Identify the preparation type.
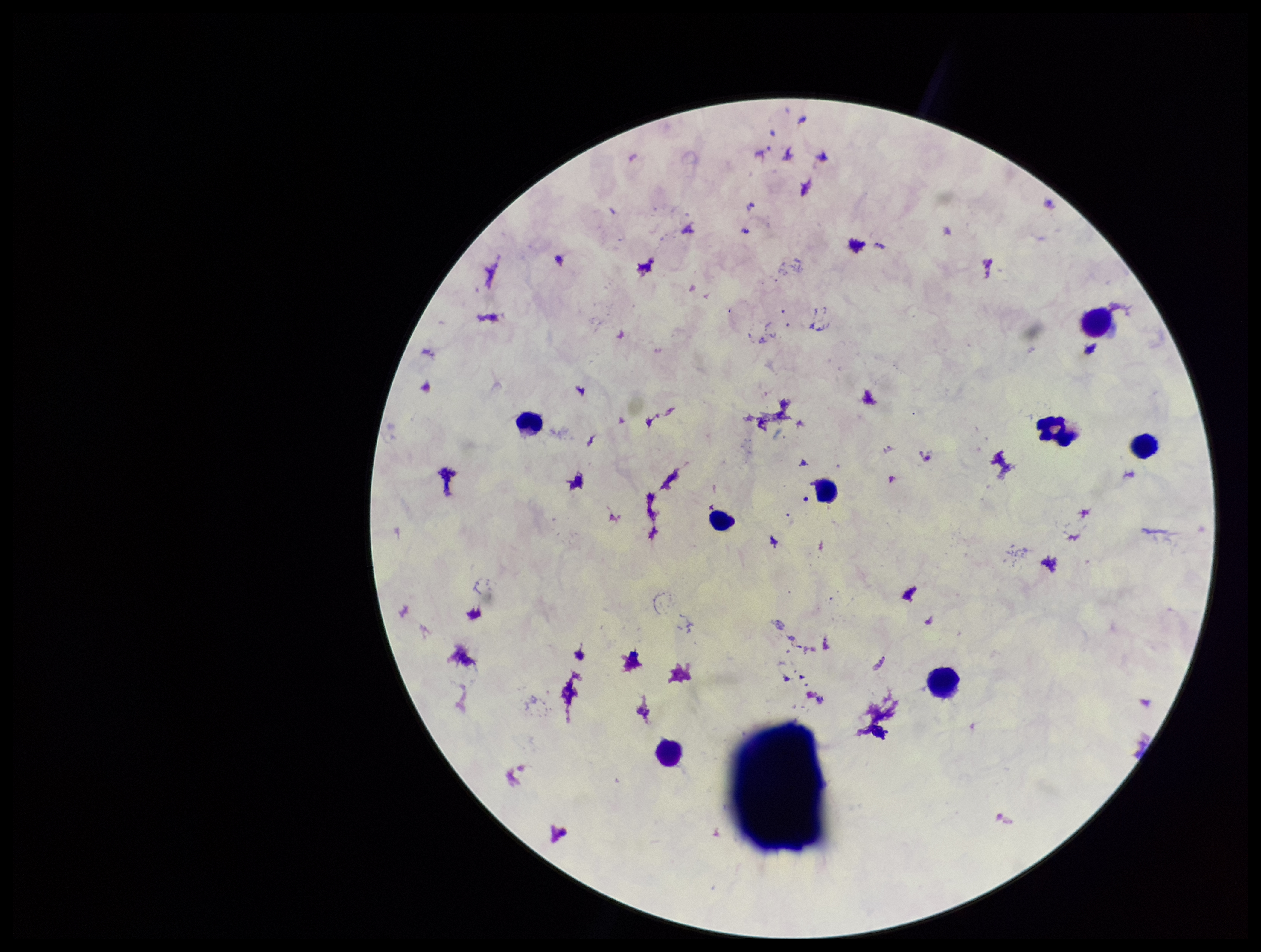
A thick smear.

Summary:
  - Field of view: single
  - Stain: Giemsa
  - Image size: 1261×952 pixels
  - Plasmodium parasites: none seen
  - Patient malaria status: negative
  - Parasite count: 0
  - Capture: smartphone photograph through the microscope eyepiece
  - Leukocyte count: 7